Name the parasite shown.
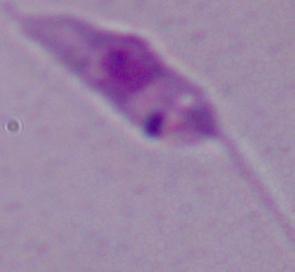
Leishmania.

Summary:
  - Modality: micrograph
  - Magnification: 1000x